Describe the morphology of the red blood cells.
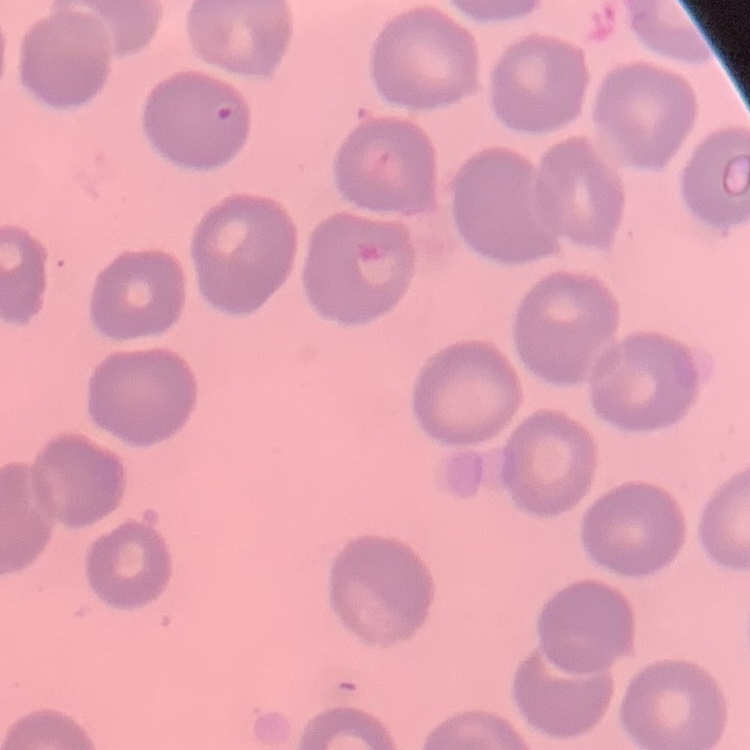
No rouleaux formation.

image_type: one tile cut from a larger photomicrograph
stain: Field's or Giemsa
preparation: thin blood film